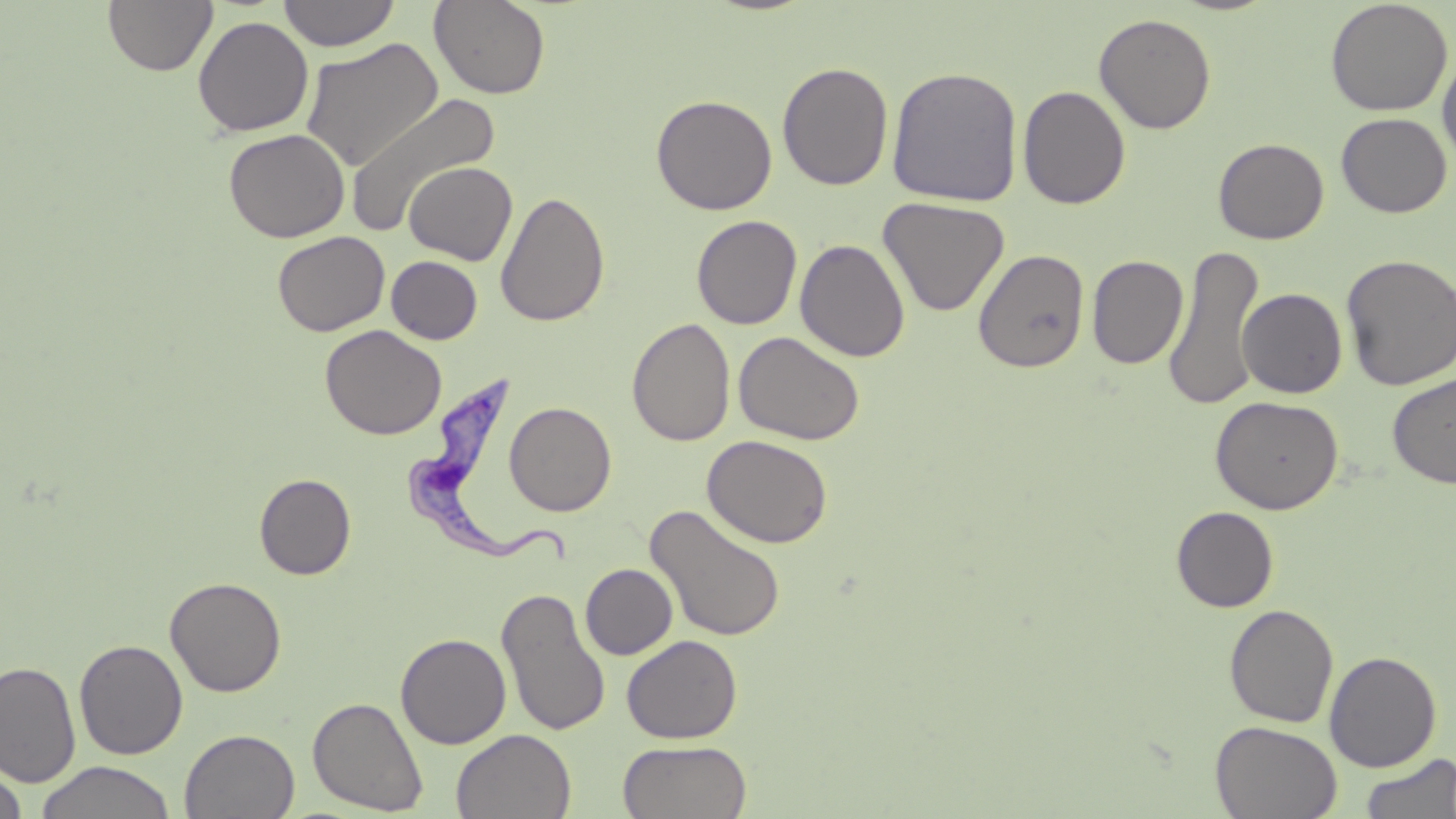
slide-level diagnosis = Trypanosoma brucei
stain = May-Grünwald-Giemsa
uninfected red blood cell locations = approximate bounding boxes as [x1, y1, x2, y2] in pixels: [103, 0, 218, 76], [278, 0, 400, 51], [428, 0, 551, 100], [1325, 0, 1453, 117], [1093, 13, 1217, 134], [192, 15, 314, 137], [300, 36, 445, 173], [1438, 48, 1456, 172], [776, 61, 894, 191], [886, 66, 1023, 207], [1017, 85, 1131, 209], [345, 92, 500, 238], [651, 94, 777, 215], [1336, 113, 1452, 218], [223, 128, 350, 243], [1213, 138, 1329, 244], [404, 161, 517, 265], [495, 191, 610, 327], [878, 197, 1009, 317], [691, 214, 802, 330], [272, 230, 390, 336], [795, 239, 911, 362], [1164, 244, 1265, 411], [973, 248, 1091, 373], [1340, 254, 1456, 391], [386, 255, 482, 344], [1086, 255, 1188, 370], [1237, 288, 1347, 398], [626, 317, 736, 446], [320, 325, 446, 440], [733, 331, 865, 446], [1387, 372, 1456, 488], [1210, 395, 1344, 515], [504, 401, 617, 516], [702, 434, 833, 549], [254, 473, 356, 580], [644, 504, 787, 642], [1171, 506, 1279, 612], [580, 563, 678, 659], [165, 577, 287, 697], [496, 586, 611, 738], [1224, 604, 1339, 727], [395, 632, 511, 749], [622, 635, 743, 743], [74, 639, 188, 760], [1324, 650, 1442, 772], [0, 661, 80, 788], [307, 696, 429, 815], [1210, 720, 1342, 819], [180, 728, 300, 819], [452, 729, 576, 819], [618, 739, 752, 819], [1357, 753, 1456, 819], [35, 761, 177, 819], [1, 764, 29, 819]
Trypanosoma brucei locations = approximate bounding boxes as [x1, y1, x2, y2] in pixels: [400, 372, 572, 569]
field of view = one of a larger specimen
preparation = thin blood film
modality = light microscopy
magnification = 1000x
image size = 1456×819 pixels